Outline each blood parasite and name the species.
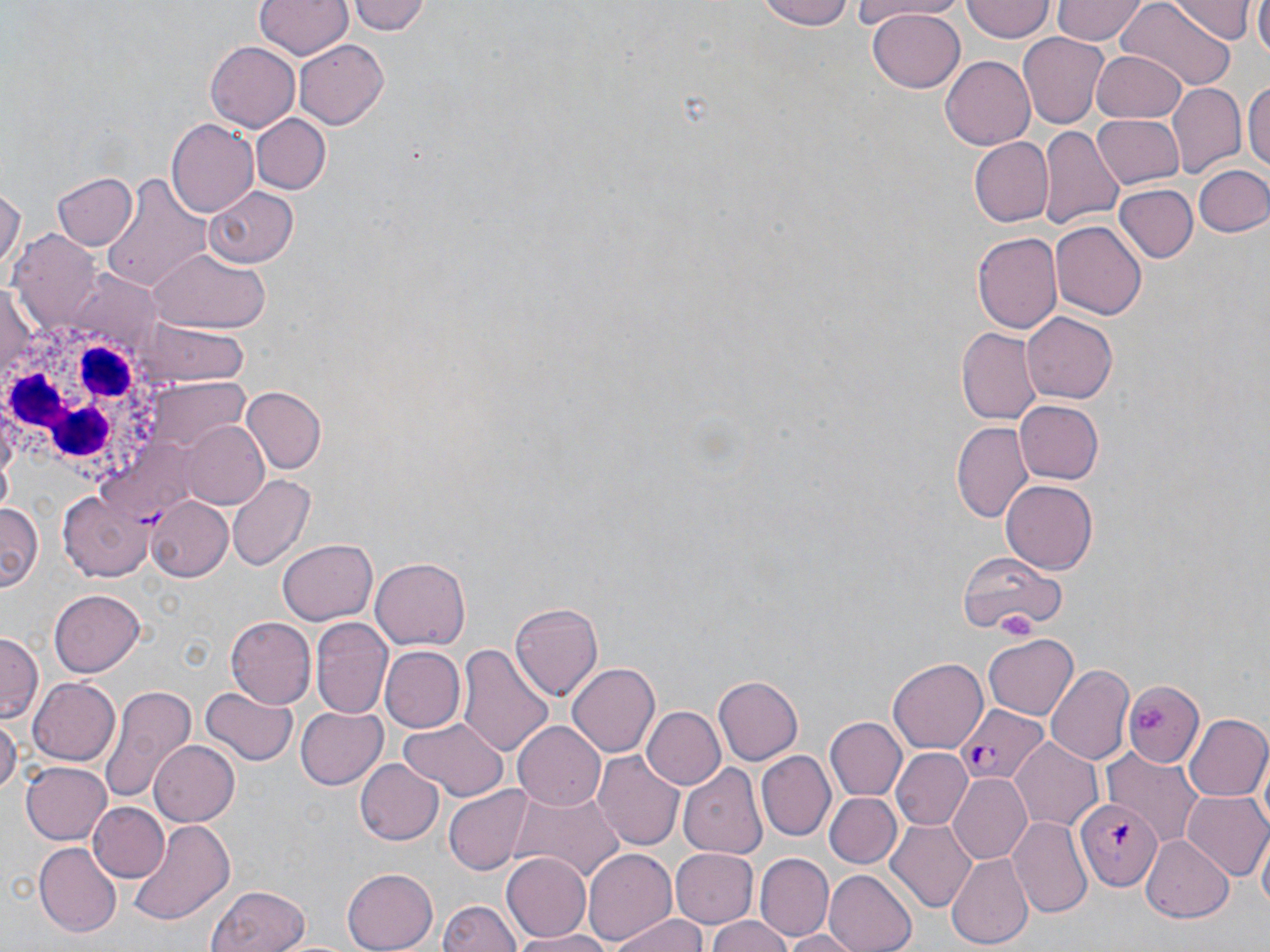

Approximate bounding boxes as named x1/y1/x2/y2 corners in pixels.
Plasmodium falciparum-infected red blood cells: (x1=958, y1=705, x2=1046, y2=784), (x1=1075, y1=796, x2=1162, y2=890).
No Plasmodium ovale, Plasmodium malariae, Plasmodium vivax, Babesia divergens, or Trypanosoma brucei observed.

Platelet locations: (x1=999, y1=614, x2=1037, y2=642), (x1=1136, y1=703, x2=1171, y2=734). White blood cell locations: (x1=0, y1=301, x2=187, y2=503). Uninfected red blood cell locations: (x1=255, y1=0, x2=351, y2=59), (x1=350, y1=0, x2=431, y2=36), (x1=754, y1=0, x2=857, y2=30), (x1=851, y1=0, x2=972, y2=21), (x1=962, y1=0, x2=1053, y2=42), (x1=1054, y1=0, x2=1145, y2=44), (x1=1166, y1=0, x2=1254, y2=41), (x1=1253, y1=0, x2=1270, y2=59), (x1=1119, y1=3, x2=1234, y2=90), (x1=867, y1=7, x2=965, y2=91), (x1=1017, y1=34, x2=1109, y2=126), (x1=294, y1=39, x2=388, y2=130), (x1=205, y1=40, x2=304, y2=131), (x1=1090, y1=49, x2=1187, y2=121), (x1=941, y1=55, x2=1036, y2=150), (x1=1245, y1=75, x2=1270, y2=178), (x1=1168, y1=82, x2=1244, y2=177), (x1=1090, y1=113, x2=1184, y2=189), (x1=250, y1=114, x2=331, y2=195), (x1=167, y1=119, x2=260, y2=218), (x1=1039, y1=127, x2=1122, y2=233), (x1=967, y1=137, x2=1054, y2=227), (x1=1193, y1=164, x2=1270, y2=237), (x1=52, y1=171, x2=136, y2=250), (x1=102, y1=174, x2=213, y2=291), (x1=0, y1=184, x2=23, y2=280), (x1=1115, y1=185, x2=1196, y2=264), (x1=204, y1=186, x2=299, y2=267), (x1=1050, y1=220, x2=1147, y2=321), (x1=971, y1=229, x2=1063, y2=331), (x1=11, y1=233, x2=102, y2=336), (x1=150, y1=246, x2=271, y2=333), (x1=1, y1=282, x2=43, y2=387), (x1=1021, y1=312, x2=1118, y2=405), (x1=143, y1=321, x2=248, y2=384), (x1=957, y1=328, x2=1041, y2=423), (x1=241, y1=385, x2=327, y2=473), (x1=1012, y1=399, x2=1103, y2=484), (x1=182, y1=420, x2=271, y2=510), (x1=951, y1=422, x2=1034, y2=524), (x1=229, y1=474, x2=317, y2=572), (x1=1001, y1=480, x2=1098, y2=574), (x1=59, y1=487, x2=153, y2=583), (x1=143, y1=493, x2=233, y2=580), (x1=0, y1=502, x2=41, y2=592), (x1=276, y1=540, x2=375, y2=625), (x1=963, y1=547, x2=1064, y2=636), (x1=371, y1=556, x2=471, y2=650), (x1=49, y1=589, x2=147, y2=677), (x1=511, y1=602, x2=602, y2=699), (x1=312, y1=615, x2=394, y2=721), (x1=227, y1=617, x2=317, y2=708), (x1=1, y1=633, x2=40, y2=723), (x1=984, y1=635, x2=1080, y2=721), (x1=459, y1=643, x2=555, y2=758), (x1=379, y1=646, x2=464, y2=734), (x1=889, y1=659, x2=987, y2=751), (x1=566, y1=663, x2=659, y2=758), (x1=1045, y1=663, x2=1134, y2=764), (x1=26, y1=676, x2=119, y2=766), (x1=711, y1=676, x2=802, y2=766), (x1=1124, y1=682, x2=1205, y2=767), (x1=98, y1=683, x2=198, y2=806), (x1=201, y1=685, x2=298, y2=766), (x1=296, y1=704, x2=388, y2=788), (x1=643, y1=707, x2=724, y2=789), (x1=0, y1=713, x2=18, y2=801), (x1=1184, y1=714, x2=1270, y2=803), (x1=824, y1=715, x2=906, y2=798), (x1=396, y1=716, x2=507, y2=800), (x1=514, y1=720, x2=608, y2=810), (x1=1010, y1=738, x2=1102, y2=830), (x1=148, y1=740, x2=240, y2=827), (x1=890, y1=749, x2=971, y2=831), (x1=1104, y1=749, x2=1204, y2=845), (x1=593, y1=752, x2=687, y2=852), (x1=758, y1=752, x2=834, y2=839), (x1=357, y1=759, x2=443, y2=846), (x1=20, y1=762, x2=113, y2=845), (x1=678, y1=763, x2=767, y2=860), (x1=948, y1=773, x2=1032, y2=865), (x1=444, y1=786, x2=533, y2=874), (x1=512, y1=791, x2=623, y2=884), (x1=825, y1=792, x2=901, y2=869), (x1=1183, y1=792, x2=1270, y2=881), (x1=90, y1=804, x2=168, y2=882), (x1=129, y1=817, x2=233, y2=922), (x1=1010, y1=817, x2=1093, y2=918), (x1=886, y1=820, x2=975, y2=913), (x1=1255, y1=829, x2=1269, y2=915), (x1=1140, y1=834, x2=1234, y2=920), (x1=34, y1=843, x2=122, y2=936), (x1=582, y1=847, x2=677, y2=948), (x1=671, y1=849, x2=758, y2=926), (x1=500, y1=852, x2=591, y2=942), (x1=948, y1=852, x2=1032, y2=949), (x1=758, y1=853, x2=834, y2=940), (x1=822, y1=867, x2=917, y2=952), (x1=343, y1=868, x2=437, y2=951), (x1=209, y1=886, x2=312, y2=952), (x1=439, y1=898, x2=524, y2=952), (x1=611, y1=912, x2=711, y2=952), (x1=706, y1=917, x2=797, y2=952), (x1=775, y1=928, x2=864, y2=951), (x1=512, y1=930, x2=617, y2=951). Slide-level diagnosis: Plasmodium falciparum. Optical microscopy. Captured at 1000x magnification. Image is 1270×952 pixels. Thin blood film. May-Grünwald-Giemsa-stained preparation. Single field of view.